Identify the parasite.
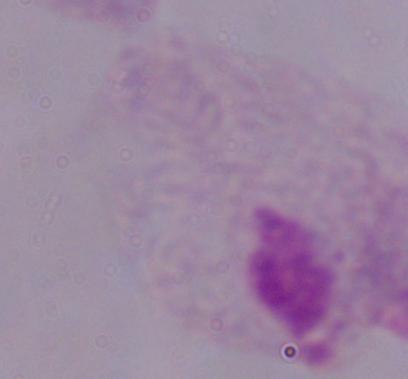

This is a trichomonad.

modality: micrograph
magnification: 1000x